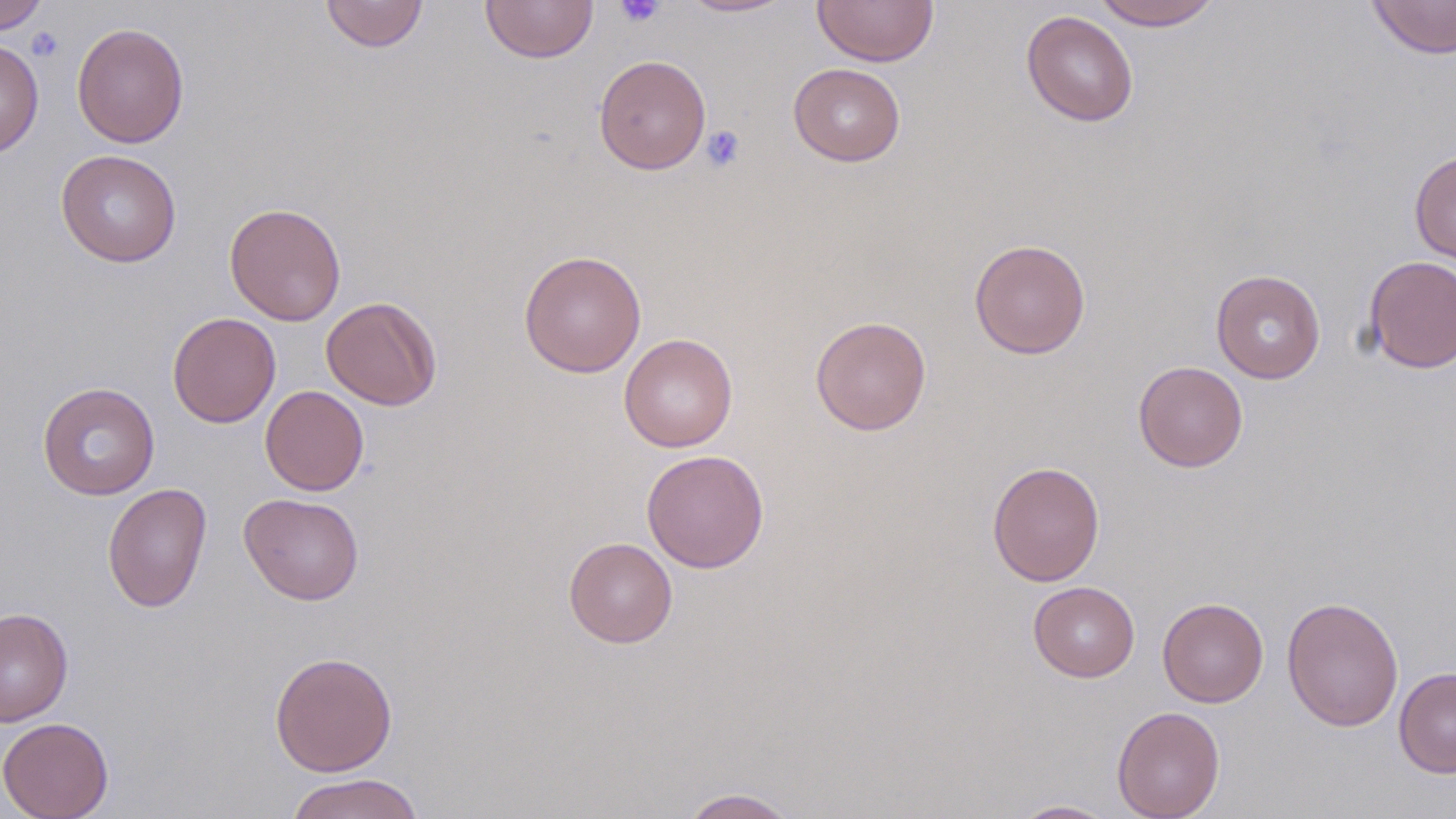

Approximate bounding boxes as named x1/y1/x2/y2 corners in pixels. Platelet locations: (x1=615, y1=0, x2=665, y2=28), (x1=26, y1=27, x2=64, y2=62), (x1=702, y1=125, x2=746, y2=172). Uninfected red blood cell locations: (x1=0, y1=0, x2=47, y2=34), (x1=319, y1=0, x2=429, y2=53), (x1=481, y1=0, x2=598, y2=63), (x1=678, y1=0, x2=795, y2=18), (x1=1091, y1=0, x2=1222, y2=30), (x1=1366, y1=0, x2=1456, y2=59), (x1=812, y1=1, x2=939, y2=67), (x1=1021, y1=10, x2=1138, y2=127), (x1=72, y1=22, x2=190, y2=148), (x1=0, y1=39, x2=44, y2=158), (x1=593, y1=54, x2=711, y2=174), (x1=788, y1=63, x2=906, y2=167), (x1=55, y1=149, x2=182, y2=267), (x1=1409, y1=149, x2=1456, y2=266), (x1=224, y1=203, x2=347, y2=326), (x1=969, y1=238, x2=1091, y2=359), (x1=518, y1=250, x2=647, y2=378), (x1=1362, y1=255, x2=1456, y2=373), (x1=1211, y1=269, x2=1326, y2=383), (x1=321, y1=296, x2=442, y2=410), (x1=167, y1=312, x2=281, y2=428), (x1=809, y1=316, x2=931, y2=435), (x1=618, y1=333, x2=738, y2=452), (x1=1133, y1=361, x2=1248, y2=472), (x1=37, y1=381, x2=160, y2=500), (x1=260, y1=385, x2=369, y2=496), (x1=641, y1=450, x2=769, y2=573), (x1=987, y1=460, x2=1105, y2=586), (x1=103, y1=482, x2=212, y2=613), (x1=239, y1=493, x2=365, y2=605), (x1=563, y1=537, x2=677, y2=648), (x1=1027, y1=581, x2=1140, y2=682), (x1=1281, y1=596, x2=1404, y2=732), (x1=1157, y1=597, x2=1269, y2=708), (x1=0, y1=607, x2=74, y2=727), (x1=269, y1=651, x2=398, y2=777), (x1=1393, y1=667, x2=1456, y2=778), (x1=1111, y1=706, x2=1225, y2=819), (x1=0, y1=716, x2=114, y2=819), (x1=285, y1=772, x2=425, y2=819), (x1=678, y1=787, x2=799, y2=818), (x1=1009, y1=799, x2=1120, y2=818). Slide-level diagnosis: negative for blood parasites. Optical microscopy. May-Grünwald-Giemsa stain. Single field of view. Thin blood smear. Image is 1456×819 pixels. 1000x magnification.